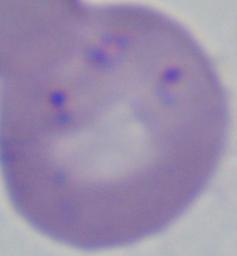

{
  "identification": "Babesia",
  "magnification": "1000x",
  "modality": "micrograph"
}